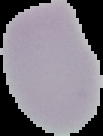
image size = 103×136 pixels
image type = segmented cell region with the area outside set to black
malaria status = uninfected
preparation = thin blood film